Locate every Plasmodium parasite and every leukocyte.
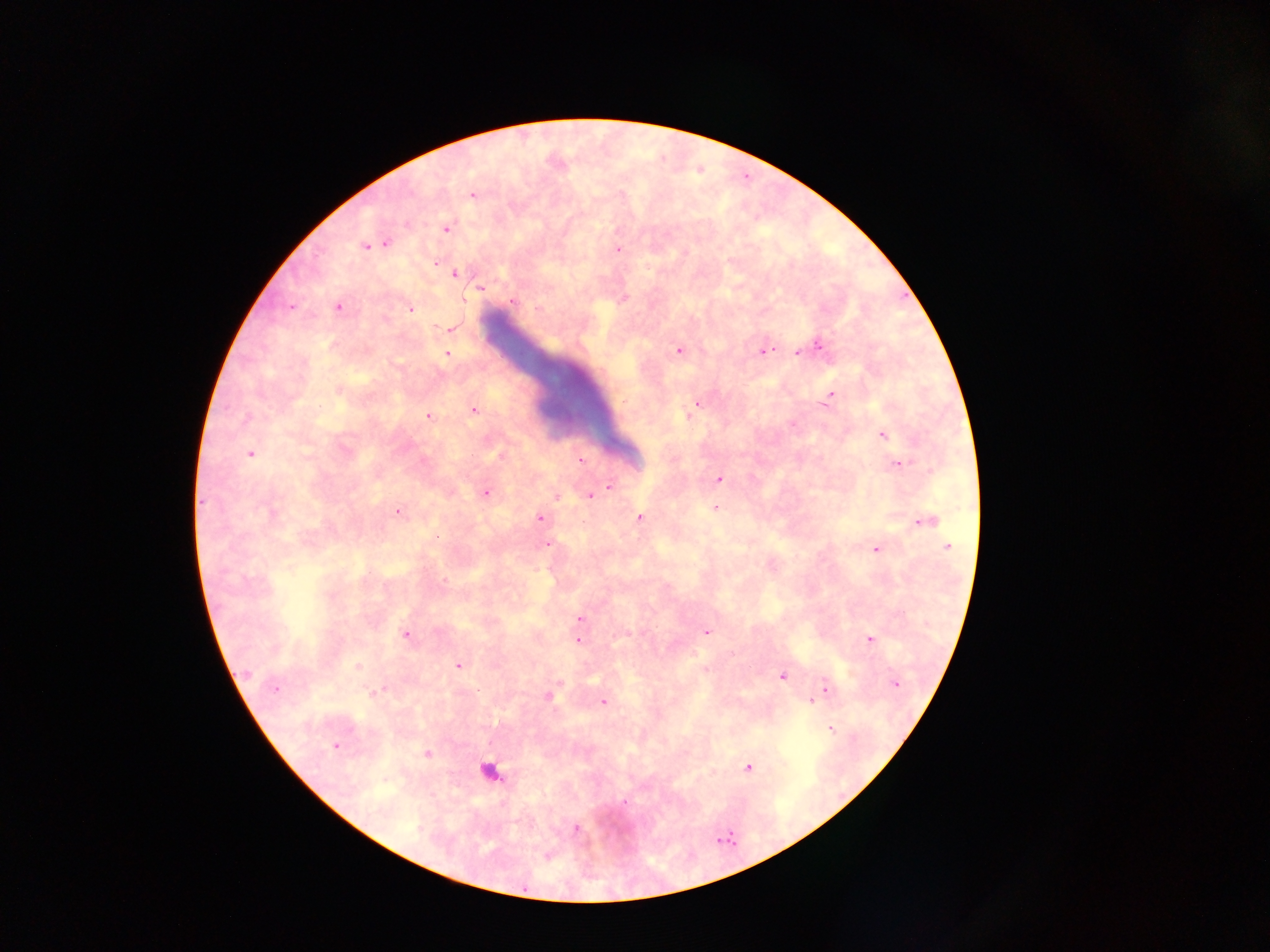

Approximate centers as x y in pixels.
Plasmodium parasites: 472 194; 446 228; 385 244; 374 245; 366 246; 618 249; 434 262; 455 273; 479 289; 623 298; 511 300; 338 306; 290 307; 411 308; 450 328; 817 345; 679 350; 762 351; 798 351; 447 354; 338 390; 830 397; 697 402; 473 410; 689 412; 429 416; 883 434; 250 453; 501 455; 580 460; 897 463; 719 479; 608 486; 485 493; 556 495; 589 495; 715 508; 397 511; 540 517; 639 518; 924 521; 548 543; 948 546; 875 549; 579 618; 706 631; 405 635; 869 639; 578 640; 459 665; 357 666; 705 670; 782 676; 894 683; 274 688; 824 688; 548 696; 603 701; 811 701; 830 729; 336 745; 427 753; 748 767; 623 802; 575 829; 546 855.
Leukocytes: 489 771.

Collected in Ghana. Image is 1270×952 pixels. Mobile-phone photograph taken through the microscope. Single field of view. Thick blood film.